Report the malaria status of this cell.
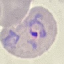

It is parasitized.

Summary:
  - Capture: smartphone camera at the microscope eyepiece
  - Preparation: thin blood film
  - Stain: Giemsa
  - Image type: automatically extracted cell patch, resized to 64 × 64 pixels